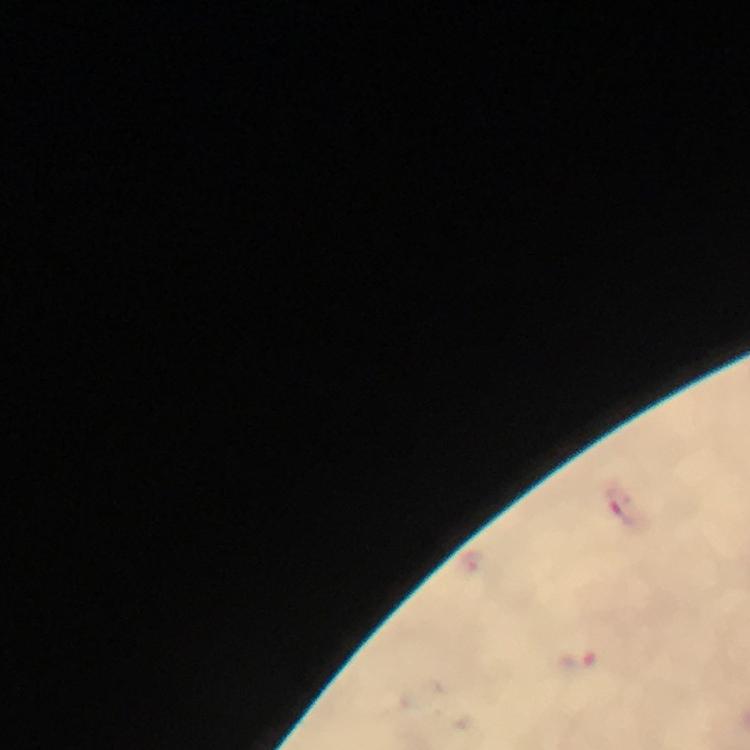
Approximate centers as [x, y] in pixels.
Summary:
  - Malaria parasite locations: [628, 509], [577, 664]
  - Image size: 750×750 pixels
  - Magnification: 100x
  - Cropped from: one field of view
  - Immersion oil: used
  - Capture: smartphone camera through the microscope
  - Preparation: thick smear
  - Context: from a malaria diagnostic workup
  - Stain: Giemsa